Identify the parasite.
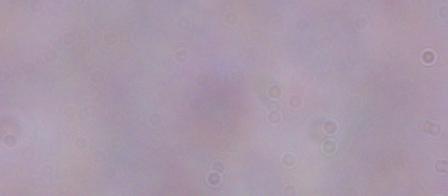

A trypanosome.

Photomicrograph. Captured at 1000x magnification.